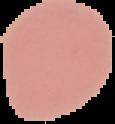

image size = 115×124 pixels
result = negative for malaria parasites
preparation = thin blood smear
image type = segmented cell region on a black background